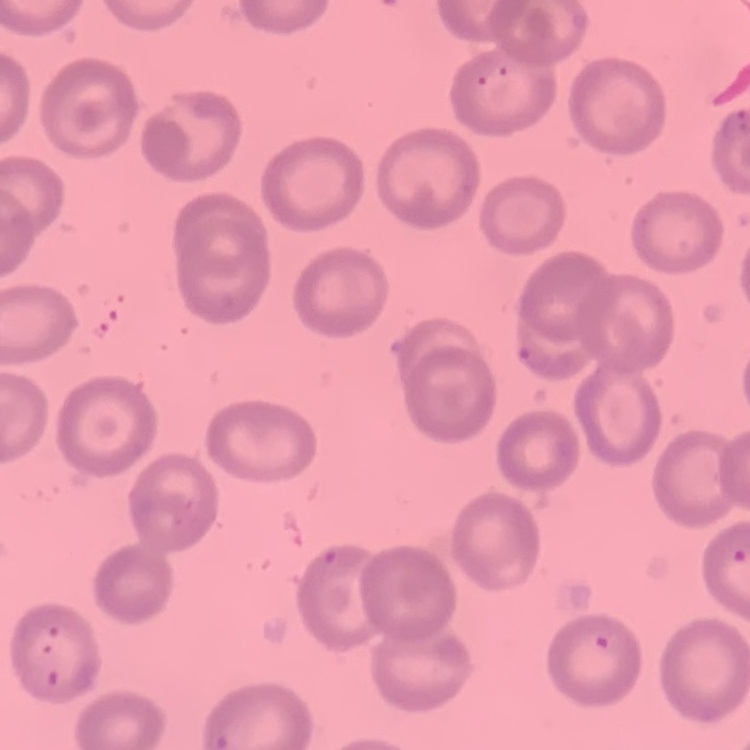

Summary:
  - Erythrocyte morphology: no rouleaux formation
  - Stain: Field's or Giemsa
  - Image type: one tile cut from a larger photomicrograph
  - Preparation: thin peripheral smear